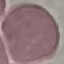
Malaria status: uninfected. Giemsa stain. Automatically extracted cell patch, resized to 64 × 64 pixels. Thin blood smear. Photographed with a smartphone camera at the microscope eyepiece.